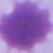
modality = photomicrograph
magnification = 1000x
identification = erythrocyte